Identify the blood parasite species.
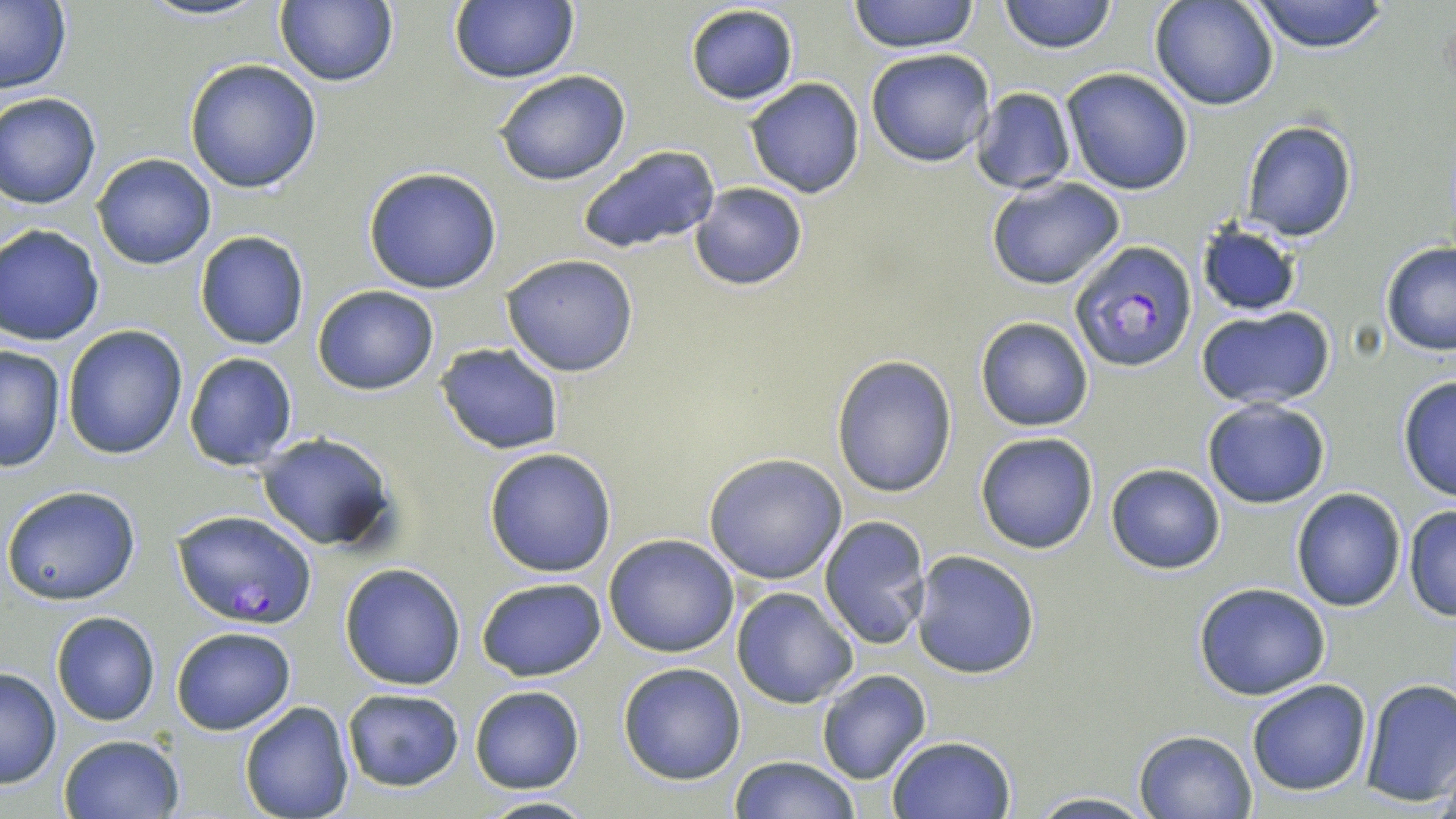
Plasmodium falciparum.

Summary:
  - Coordinate format: approximate bounding boxes as [x1, y1, x2, y2] in pixels
  - Plasmodium falciparum-infected red blood cell locations: [1070, 240, 1197, 373], [173, 509, 314, 627]
  - Uninfected red blood cell locations: [138, 0, 271, 21], [276, 0, 398, 87], [451, 0, 580, 84], [848, 0, 980, 53], [998, 0, 1116, 53], [1247, 0, 1392, 53], [1151, 1, 1277, 110], [0, 2, 73, 94], [683, 4, 799, 105], [867, 48, 997, 167], [184, 58, 324, 194], [1061, 68, 1193, 195], [493, 70, 631, 185], [745, 77, 865, 198], [971, 87, 1075, 194], [1, 94, 101, 209], [1240, 120, 1358, 241], [576, 145, 721, 256], [92, 153, 216, 269], [364, 167, 504, 295], [986, 175, 1127, 291], [689, 182, 809, 291], [1195, 222, 1304, 316], [1, 224, 105, 346], [194, 231, 309, 350], [1380, 243, 1456, 358], [501, 253, 638, 377], [312, 284, 439, 395], [1194, 306, 1337, 410], [975, 316, 1093, 431], [62, 325, 188, 460], [436, 342, 565, 454], [0, 343, 67, 470], [183, 352, 298, 470], [833, 355, 957, 498], [1397, 375, 1456, 502], [1201, 397, 1331, 508], [254, 432, 401, 555], [974, 432, 1100, 554], [483, 447, 618, 577], [702, 453, 847, 585], [1105, 463, 1225, 574], [2, 485, 144, 606], [1292, 487, 1407, 611], [1404, 505, 1456, 621], [819, 514, 933, 650], [604, 532, 739, 658], [913, 551, 1040, 679], [339, 563, 465, 689], [476, 577, 606, 680], [1193, 581, 1330, 700], [731, 586, 859, 709], [50, 610, 161, 727], [170, 625, 297, 735], [618, 662, 746, 784], [0, 668, 61, 788], [816, 669, 931, 785], [1244, 678, 1372, 796], [1360, 679, 1456, 807], [469, 686, 584, 793], [340, 687, 465, 792], [239, 701, 354, 819], [1133, 728, 1258, 818], [58, 733, 185, 819], [887, 734, 1016, 819], [727, 755, 862, 818], [1021, 792, 1159, 819], [476, 796, 600, 819]
  - Stain: May-Grünwald-Giemsa
  - Magnification: 1000x
  - Modality: optical microscopy
  - Preparation: thin blood film
  - Image size: 1456×819 pixels
  - Field of view: one of a larger specimen